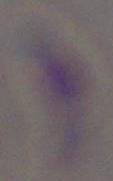

Summary:
  - Identification: Toxoplasma gondii
  - Modality: photomicrograph
  - Magnification: 1000x